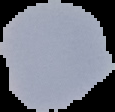

Summary:
  - Preparation: thin blood smear
  - Image size: 115×112 pixels
  - Image type: cell region segmented out of the field of view; surrounding area masked to black
  - Malaria status: uninfected